Give the preparation type.
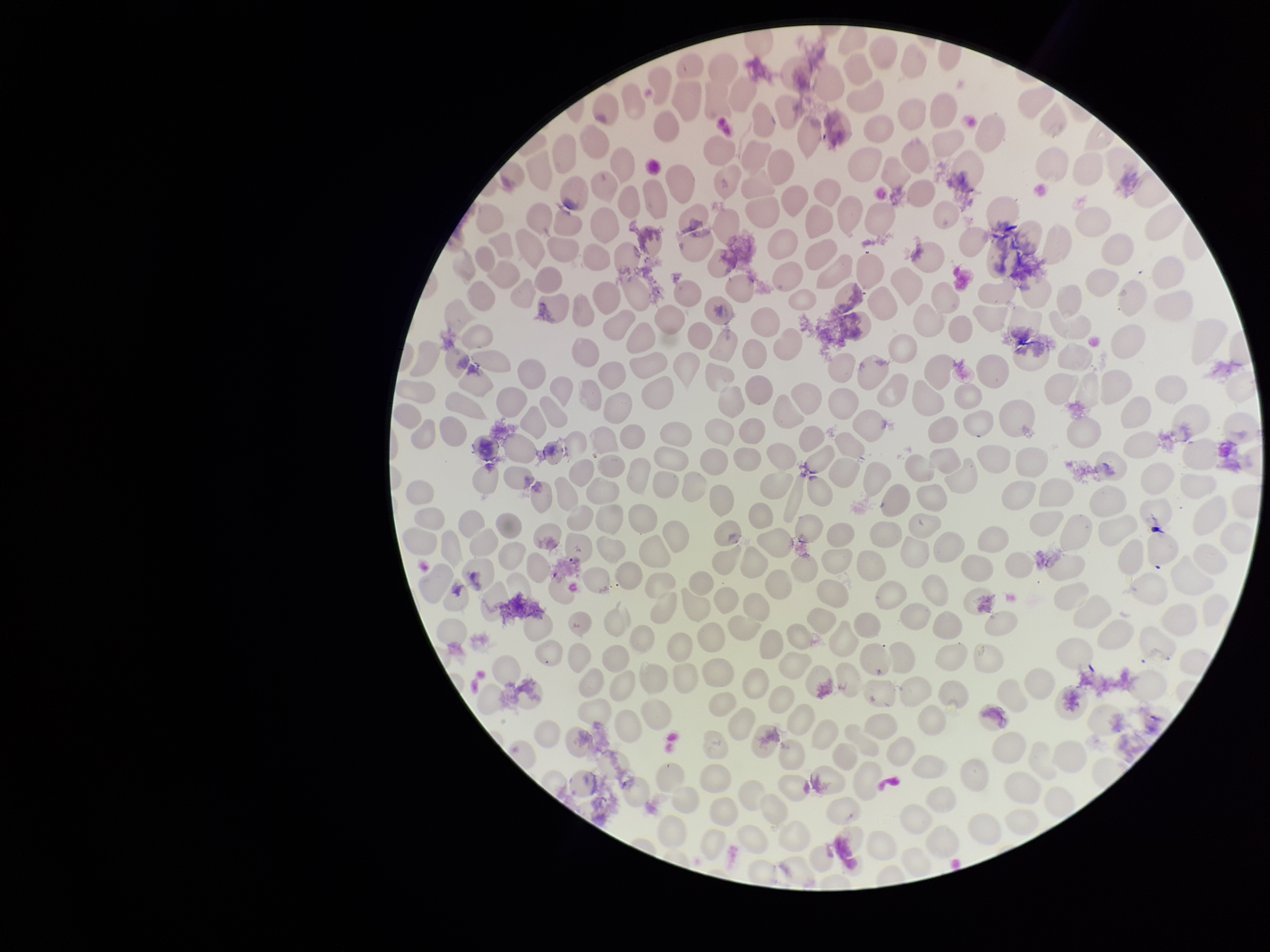
It is a thin blood smear.

capture = smartphone photograph through the microscope eyepiece
stain = Giemsa
field of view = single
patient malaria status = negative
parasitized red blood cell count = 0
parasitized red blood cells = none identified
red blood cell count = 237
image size = 1270×952 pixels